Locate every blood parasite and identify its species.
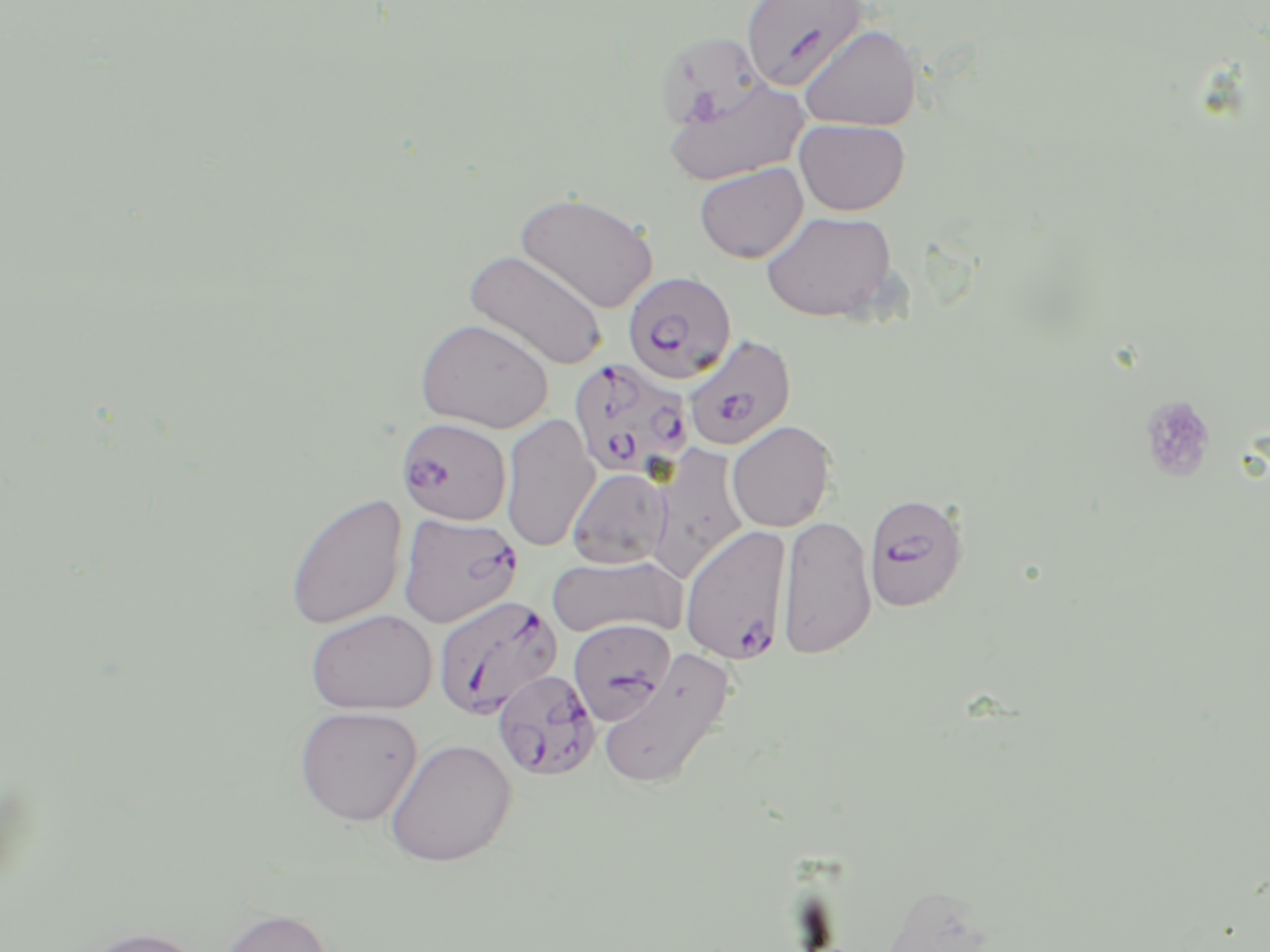

Approximate bounding boxes as [x1, y1, x2, y2] in pixels.
Plasmodium falciparum-infected red blood cells: [741, 0, 867, 91], [622, 271, 738, 384], [683, 334, 797, 451], [569, 357, 695, 481], [397, 418, 513, 525], [863, 491, 969, 612], [398, 511, 523, 628], [680, 526, 791, 664], [440, 597, 561, 718], [568, 618, 676, 725], [492, 669, 601, 781].
No Plasmodium ovale, Plasmodium malariae, Plasmodium vivax, Babesia divergens, or Trypanosoma brucei observed.

Platelet locations: [1138, 395, 1216, 482]. Uninfected red blood cell locations: [798, 25, 922, 131], [653, 31, 768, 132], [662, 76, 810, 185], [794, 118, 911, 216], [694, 163, 807, 263], [515, 192, 658, 313], [760, 210, 898, 323], [465, 249, 608, 371], [415, 317, 553, 433], [500, 414, 600, 552], [726, 420, 835, 532], [648, 446, 750, 582], [566, 467, 673, 569], [284, 491, 408, 631], [777, 515, 876, 660], [546, 554, 687, 640], [305, 609, 437, 715], [597, 650, 734, 790], [294, 705, 423, 826], [384, 738, 516, 867], [217, 907, 335, 952], [71, 925, 211, 952]. Slide-level diagnosis: Plasmodium falciparum. Light microscopy. Captured at 1000x magnification. May-Grünwald-Giemsa stain. Single field of view. Thin blood smear. Image is 1270×952 pixels.